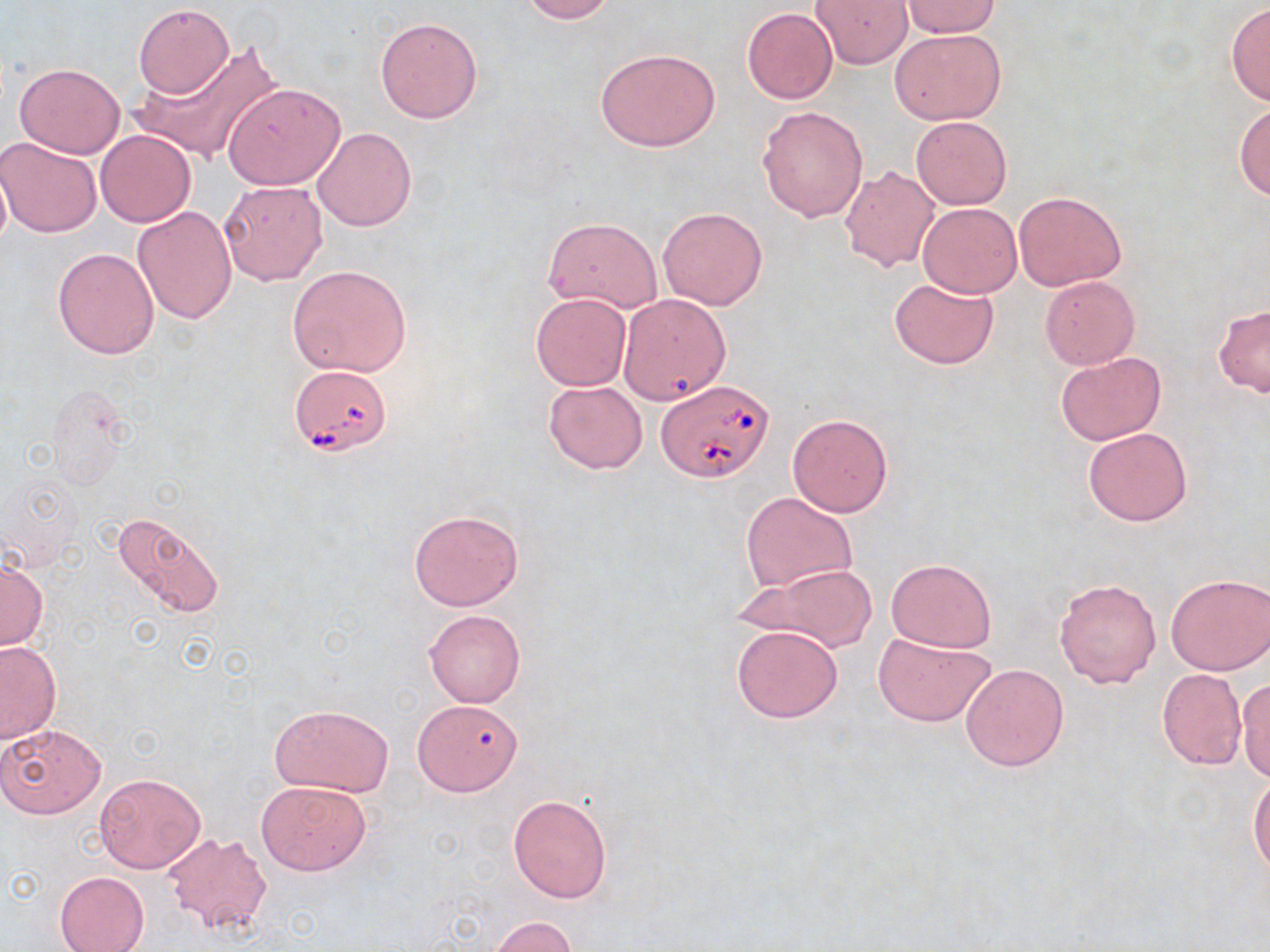
Approximate bounding boxes as (x1,y1)-(x2,y2) corner pairs in pixels. Uninfected red blood cell locations: (515,0)-(617,23), (810,0)-(913,68), (900,2)-(1001,38), (133,3)-(235,98), (1227,4)-(1270,107), (741,8)-(838,105), (375,16)-(484,123), (889,28)-(1006,124), (131,42)-(278,162), (594,47)-(722,153), (13,62)-(125,158), (223,82)-(346,190), (1234,102)-(1270,200), (757,105)-(869,222), (910,114)-(1012,210), (312,127)-(417,232), (95,129)-(197,227), (0,136)-(102,238), (0,157)-(13,254), (839,165)-(940,272), (219,180)-(329,287), (1012,191)-(1127,290), (917,202)-(1022,297), (658,205)-(769,310), (132,206)-(238,323), (542,216)-(664,313), (52,248)-(159,359), (286,264)-(414,379), (888,276)-(999,370), (1039,276)-(1139,368), (531,293)-(631,390), (618,293)-(732,406), (1213,305)-(1270,398), (1055,351)-(1166,445), (543,379)-(648,474), (787,413)-(894,517), (1083,426)-(1193,526), (742,493)-(858,594), (407,509)-(524,611), (111,512)-(226,621), (0,556)-(47,651), (885,558)-(996,652), (747,564)-(878,652), (1165,572)-(1269,676), (1053,577)-(1161,688), (424,610)-(525,707), (731,623)-(844,723), (873,632)-(996,728), (0,640)-(61,743), (960,662)-(1070,772), (1156,669)-(1246,770), (1235,674)-(1270,786), (412,698)-(524,797), (270,704)-(394,797), (0,722)-(108,819), (1249,770)-(1270,878), (95,772)-(206,873), (255,780)-(372,875), (508,794)-(612,903), (160,832)-(274,936), (54,871)-(150,952), (488,916)-(578,952). Babesia divergens-infected red blood cell locations: (288,365)-(394,456), (656,378)-(775,483). Slide-level diagnosis: Babesia divergens. One field of a larger specimen. Optical microscopy. 1000x magnification. Image is 1270×952 pixels. May-Grünwald-Giemsa stain. Thin blood smear.